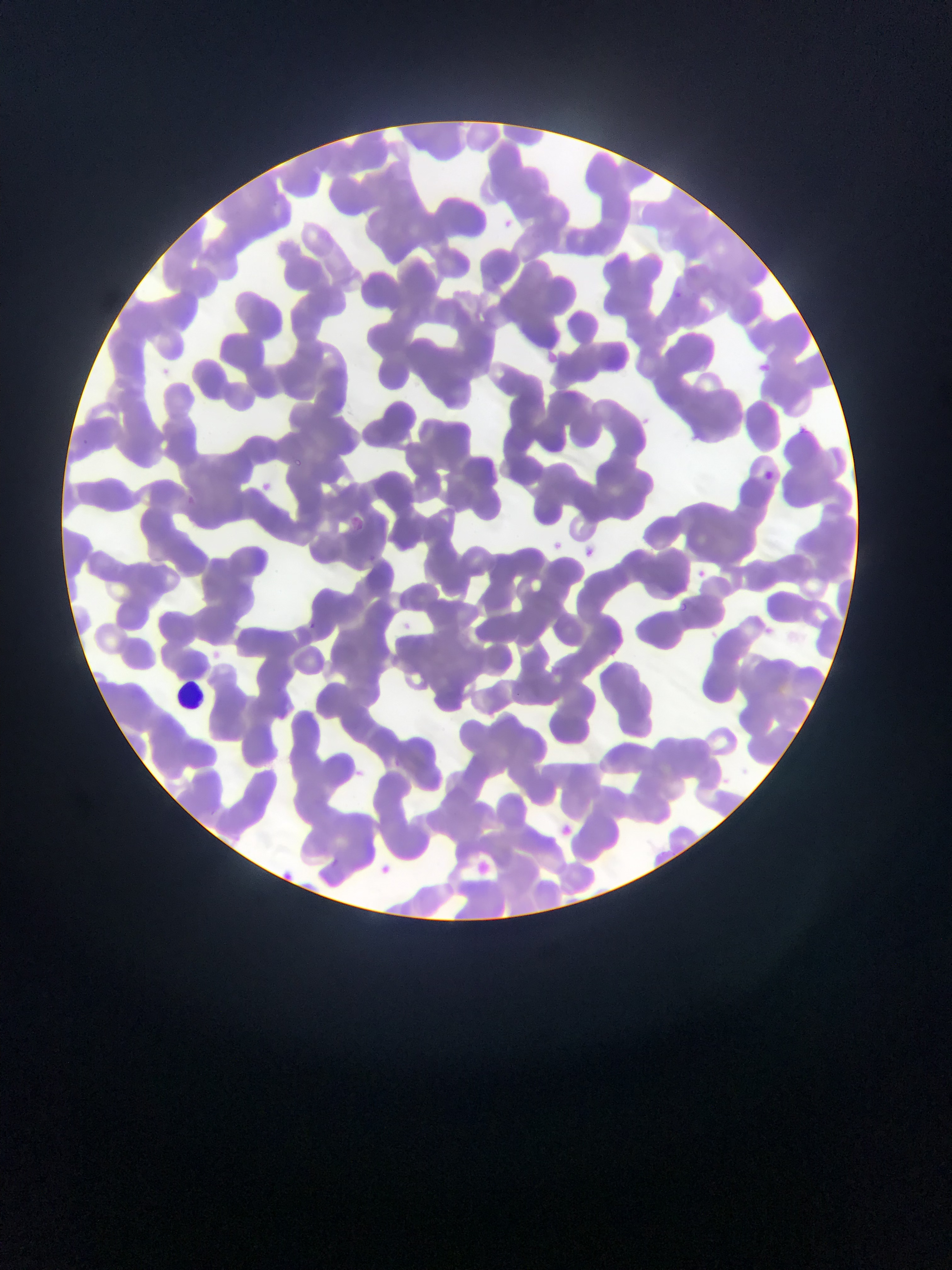
Approximate bounding boxes as left top right bottom in pixels. Leukocyte locations: 172 676 213 709. Plasmodium parasite locations: 674 288 680 299; 761 358 773 380; 795 426 805 434; 290 457 302 473; 764 467 774 480; 261 477 287 498; 350 515 380 541; 581 540 599 557; 694 565 712 579; 678 598 697 620; 304 619 327 637; 560 820 585 844; 383 858 400 881; 470 859 488 880; 274 864 288 886. One field of view. Image is 952×1270 pixels. Photographed through a microscope with a mobile-phone camera. Collected in Ghana. Thin blood film.